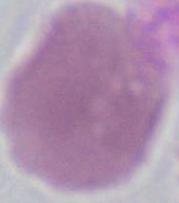

identification: erythrocyte
modality: micrograph
magnification: 1000x